Describe the morphology of the erythrocytes.
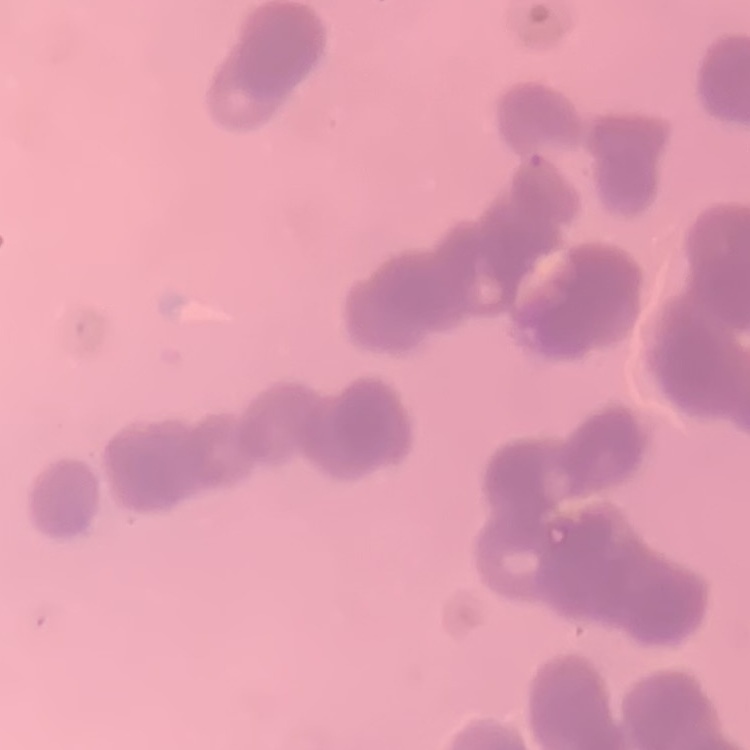
Rouleaux formation.

{
  "stain": "Field's or Giemsa",
  "preparation": "thin peripheral smear",
  "image_type": "one tile cut from a larger photomicrograph"
}